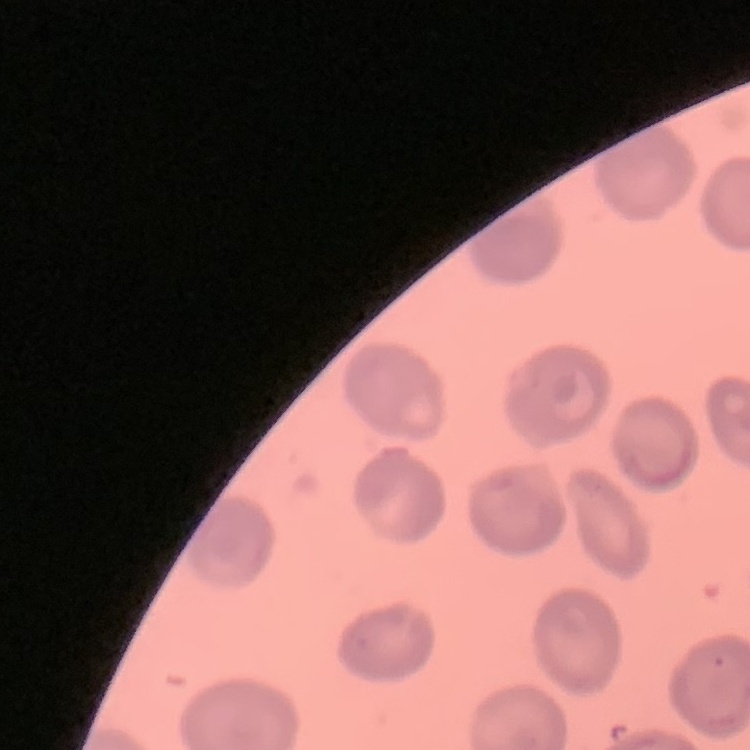
red blood cell morphology = no rouleaux formation
preparation = thin blood smear
stain = Field's or Giemsa
image type = square crop of a larger photomicrograph